Identify the cell.
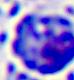
A leukocyte.

modality: photomicrograph
magnification: 400x